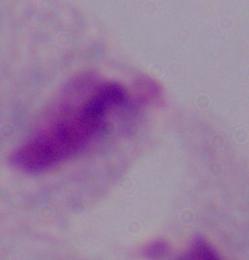
Summary:
  - Magnification: 1000x
  - Modality: micrograph
  - Identification: trichomonad